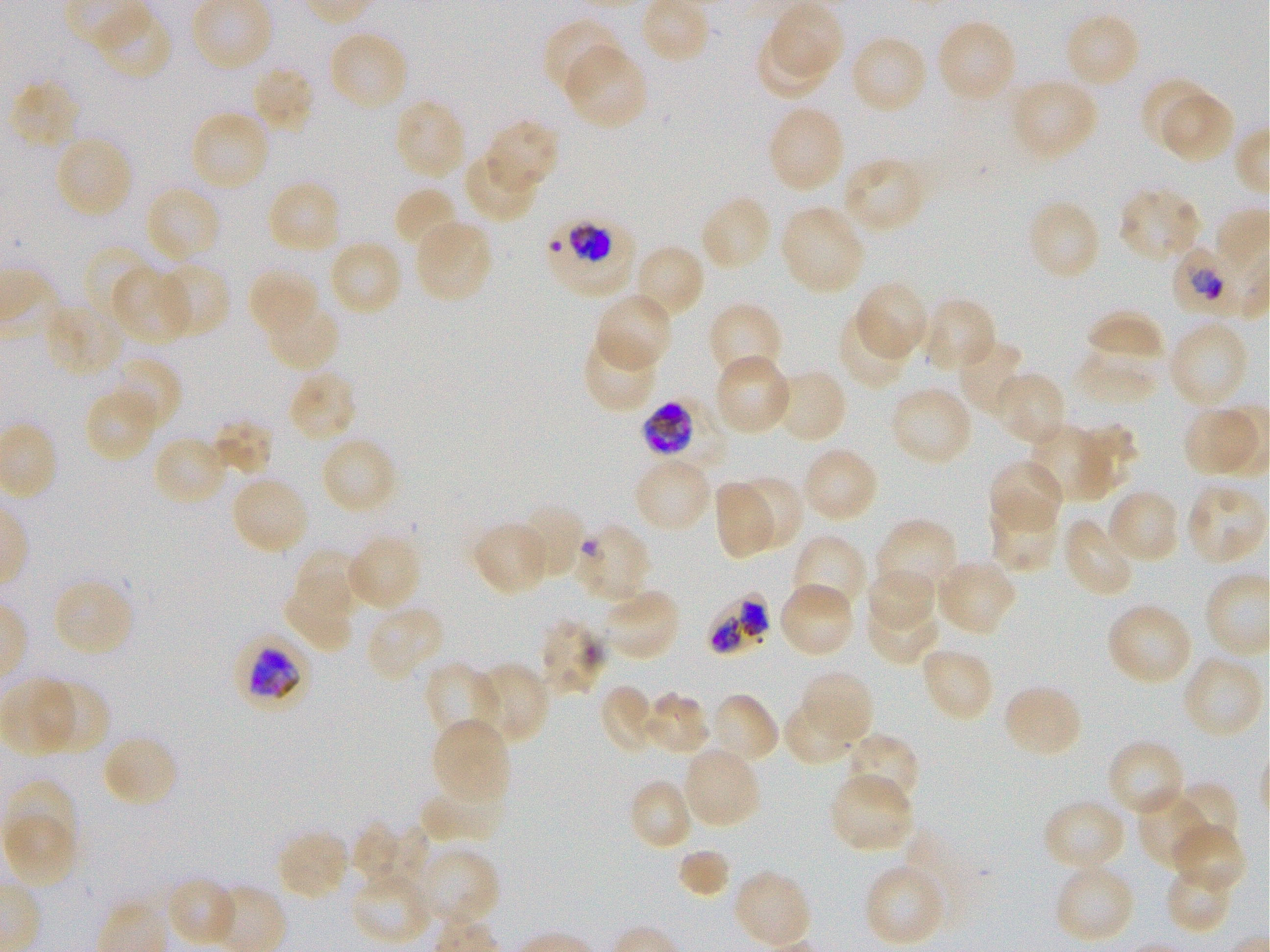
Approximate bounding boxes as {x1, y1, x2, y2} in pixels. Not every red blood cell is marked. A life-cycle stage — or a range of stages, where the recorded stages span more than one — follows each staged infected red blood cell. Locations of red blood cells of indeterminate infection status: {573, 524, 651, 604}, {542, 621, 602, 694}. Locations of infected red blood cells: {546, 215, 633, 293} trophozoite; {1173, 247, 1241, 318} trophozoite; {642, 400, 727, 471} early trophozoite to late schizont; {706, 591, 770, 658}; {235, 636, 311, 709} early trophozoite to early schizont. Locations of uninfected red blood cells: {770, 2, 843, 78}, {94, 7, 171, 82}, {1063, 11, 1141, 90}, {543, 17, 623, 99}, {936, 18, 1018, 105}, {327, 29, 410, 112}, {755, 32, 829, 100}, {850, 33, 928, 116}, {563, 45, 650, 131}, {250, 64, 316, 136}, {1011, 77, 1099, 160}, {10, 78, 81, 150}, {1141, 82, 1211, 149}, {1161, 93, 1235, 163}, {393, 98, 467, 181}, {766, 104, 846, 193}, {188, 109, 271, 191}, {485, 119, 561, 193}, {53, 135, 134, 219}, {462, 154, 539, 223}, {842, 157, 926, 234}, {266, 180, 342, 257}, {144, 184, 222, 264}, {393, 186, 461, 254}, {1117, 187, 1202, 263}, {699, 193, 773, 272}, {1026, 199, 1101, 282}, {779, 203, 868, 295}, {414, 218, 494, 304}, {327, 239, 404, 317}, {81, 243, 157, 323}, {637, 247, 705, 312}, {155, 261, 230, 339}, {109, 267, 193, 345}, {247, 267, 319, 337}, {855, 282, 929, 362}, {594, 292, 674, 374}, {922, 297, 997, 374}, {44, 298, 124, 377}, {266, 301, 343, 373}, {707, 301, 784, 383}, {1088, 309, 1166, 356}, {837, 311, 910, 390}, {1168, 318, 1251, 409}, {581, 333, 659, 412}, {958, 337, 1029, 417}, {1077, 352, 1154, 404}, {714, 355, 794, 436}, {109, 356, 182, 433}, {769, 367, 848, 445}, {287, 369, 358, 445}, {994, 372, 1067, 447}, {888, 385, 974, 468}, {84, 387, 159, 462}, {1182, 405, 1263, 479}, {209, 418, 273, 477}, {1028, 422, 1113, 500}, {1069, 423, 1137, 493}, {150, 435, 228, 507}, {319, 436, 399, 516}, {801, 446, 880, 524}, {988, 458, 1064, 534}, {636, 463, 709, 529}, {229, 475, 310, 556}, {733, 475, 803, 550}, {713, 481, 777, 560}, {1184, 483, 1267, 565}, {1106, 488, 1181, 565}, {989, 499, 1060, 572}, {518, 502, 586, 581}, {874, 517, 959, 602}, {1062, 517, 1137, 598}, {469, 520, 551, 596}, {345, 532, 422, 613}, {791, 533, 869, 617}, {300, 547, 371, 615}, {935, 557, 1017, 636}, {867, 567, 936, 635}, {51, 577, 135, 658}, {779, 582, 855, 659}, {602, 588, 682, 662}, {282, 597, 351, 650}, {864, 600, 939, 666}, {1105, 601, 1194, 686}, {366, 604, 445, 681}, {919, 646, 995, 723}, {1183, 659, 1260, 735}, {474, 661, 550, 745}, {422, 662, 501, 747}, {799, 669, 875, 744}, {2, 678, 77, 756}, {37, 679, 112, 756}, {1001, 682, 1084, 759}, {599, 684, 648, 751}, {641, 691, 710, 756}, {708, 692, 780, 766}, {783, 703, 853, 766}, {431, 718, 512, 805}, {843, 732, 921, 811}, {101, 734, 180, 810}, {1105, 738, 1186, 817}, {686, 749, 759, 825}, {829, 773, 915, 853}, {4, 780, 77, 853}, {633, 781, 690, 846}, {1168, 782, 1240, 851}, {420, 783, 507, 844}, {1137, 789, 1216, 870}, {1041, 797, 1127, 874}, {3, 812, 77, 887}, {349, 821, 398, 885}, {1171, 822, 1246, 895}, {367, 827, 433, 889}, {275, 830, 351, 902}, {418, 848, 502, 928}, {677, 849, 730, 899}, {863, 862, 946, 947}, {1052, 862, 1136, 945}, {1165, 866, 1232, 930}, {733, 868, 812, 948}, {350, 872, 435, 944}, {165, 877, 238, 947}. Thin blood film. Plasmodium falciparum strain 3D7 in static in-vitro culture. 100x oil-immersion objective, numerical aperture 1.25. Donor blood group O+. Giemsa-stained preparation. Image is 1270×952 pixels. One field from this slide.